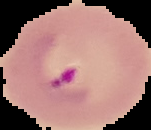

preparation = thin blood smear
image type = segmented cell region with the area outside set to black
image size = 151×130 pixels
malaria status = parasitized